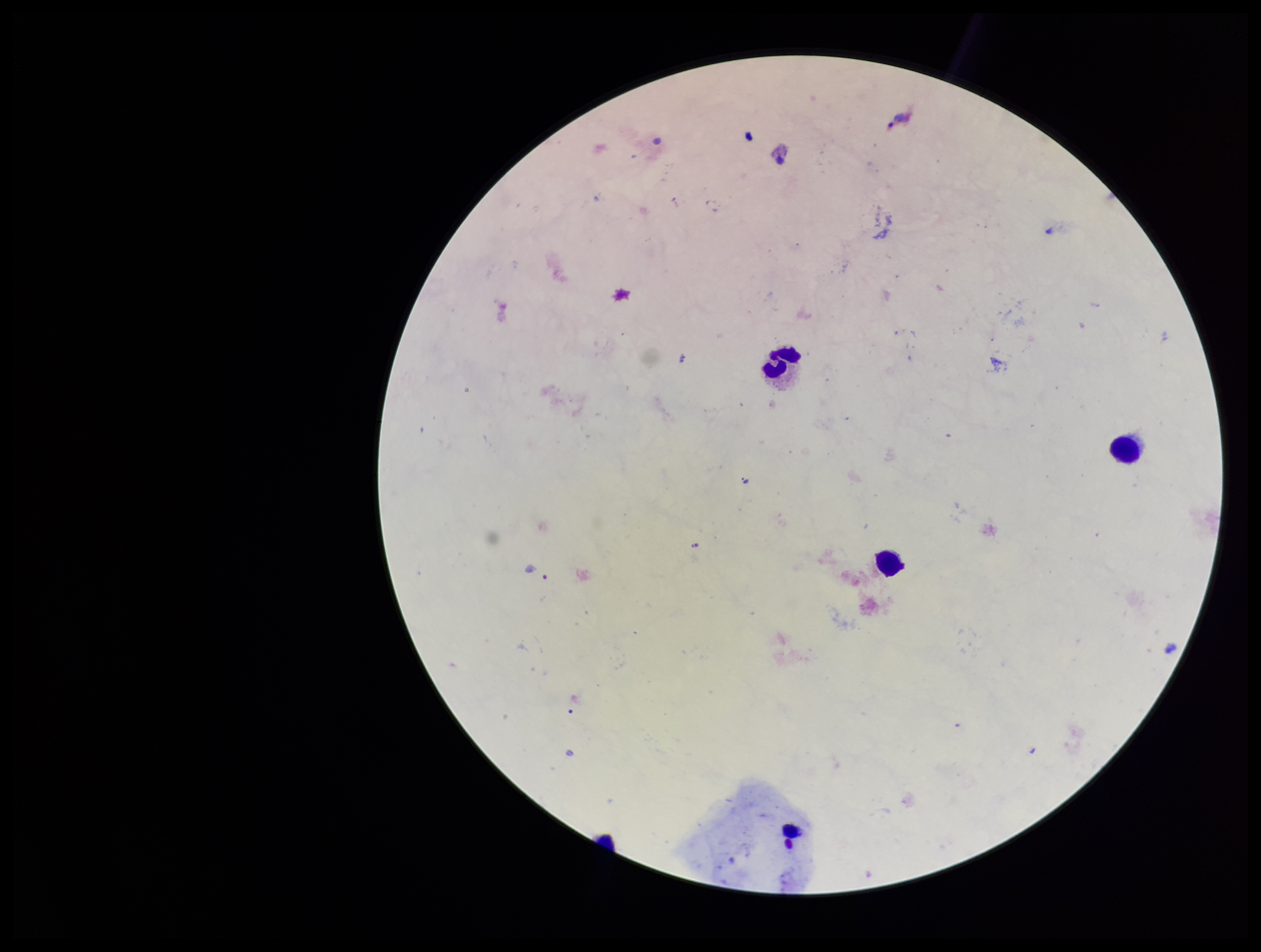
Stained with Giemsa. One field from this slide. Photographed through the microscope eyepiece with a smartphone camera. Parasite count: 0. Leukocyte count: 4. Image is 1261×952 pixels. Patient malaria status: negative. Preparation: thick. Plasmodium parasites: none detected.